Comment on the morphology of the red blood cells.
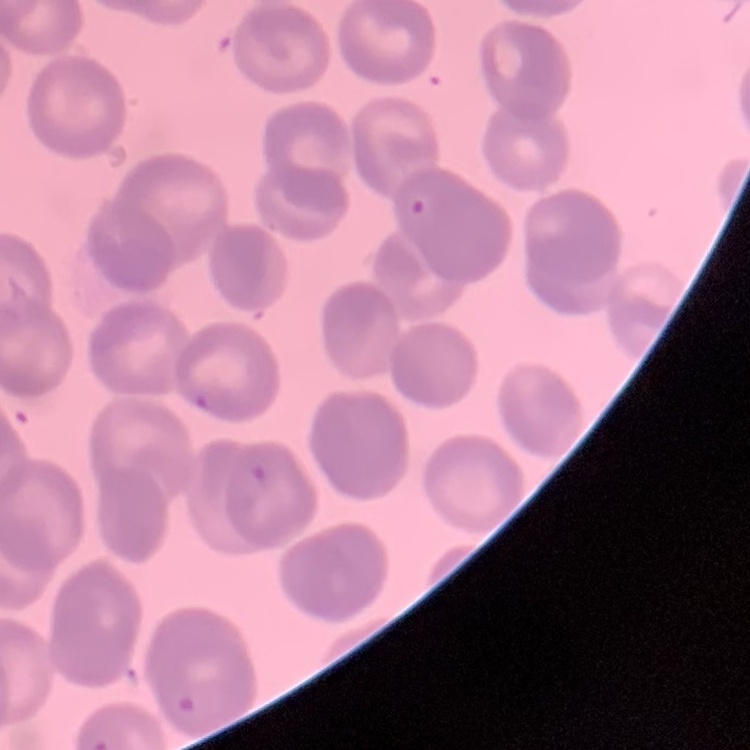

Rouleaux formation.

Summary:
  - Image type: square crop of a larger photomicrograph
  - Stain: Field's or Giemsa
  - Preparation: thin peripheral smear